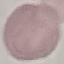

Malaria status: uninfected. Cell patch, automatically extracted from a larger field of view and resized to 64 × 64 pixels. Giemsa-stained preparation. Acquired by smartphone through the microscope eyepiece. Thin blood film.